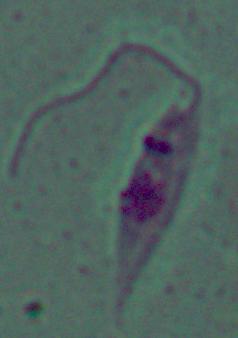 Micrograph. A Leishmania parasite is seen. 1000x magnification.